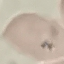
result: no malaria parasites detected
stain: Giemsa
capture: smartphone camera at the microscope eyepiece
image_type: cell patch, automatically extracted from a larger field of view and resized to 64 × 64 pixels
preparation: thin blood smear